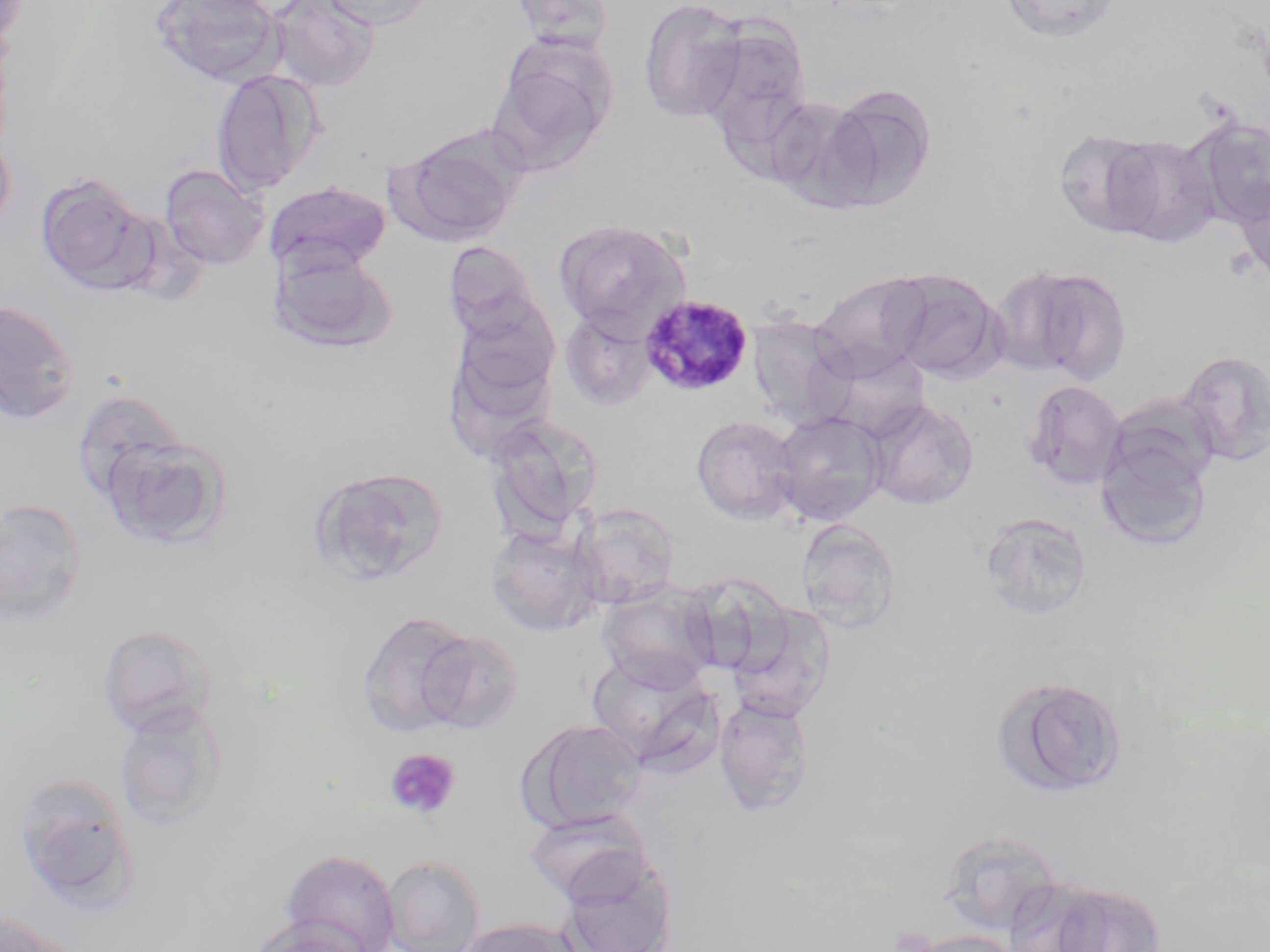

Approximate bounding boxes as (x1,y1)-(x2,y2) corner pairs in pixels. Plasmodium malariae-infected red blood cell locations: (639,294)-(754,397). Uninfected red blood cell locations: (265,0)-(380,93), (318,0)-(434,30), (509,0)-(617,53), (638,0)-(749,123), (1000,0)-(1122,43), (151,1)-(286,88), (691,17)-(813,142), (487,44)-(614,176), (211,69)-(325,195), (819,84)-(938,210), (1183,118)-(1270,228), (391,127)-(525,246), (1052,127)-(1166,238), (0,130)-(14,238), (1103,133)-(1223,247), (159,163)-(269,270), (36,173)-(159,296), (1231,175)-(1270,286), (264,180)-(391,274), (555,219)-(691,336), (443,242)-(543,342), (268,246)-(396,355), (995,264)-(1133,384), (878,268)-(1007,383), (810,272)-(934,381), (0,299)-(80,425), (560,309)-(658,410), (442,312)-(560,455), (746,314)-(856,428), (819,347)-(933,441), (1177,350)-(1270,467), (1022,380)-(1126,490), (69,387)-(195,508), (865,399)-(980,510), (771,410)-(890,526), (483,412)-(603,540), (1094,414)-(1218,552), (690,415)-(802,524), (98,433)-(229,549), (308,465)-(450,589), (0,499)-(88,628), (571,502)-(680,609), (979,511)-(1092,621), (795,518)-(902,632), (486,522)-(605,637), (677,574)-(792,679), (598,582)-(718,690), (724,602)-(836,722), (355,610)-(476,738), (97,624)-(219,737), (416,629)-(525,734), (586,650)-(721,770), (993,675)-(1130,797), (714,695)-(816,816), (114,701)-(229,831), (519,718)-(647,833), (14,772)-(136,906), (522,809)-(653,905), (937,829)-(1063,935), (281,850)-(401,952), (558,854)-(678,952), (381,855)-(486,952), (1000,878)-(1119,951), (1042,881)-(1167,951), (0,912)-(78,952), (458,917)-(585,952), (245,918)-(375,952), (907,930)-(1021,952). Platelet locations: (385,747)-(461,820), (886,928)-(938,952). Slide-level diagnosis: Plasmodium malariae. Image is 1270×952 pixels. Thin blood film. Optical microscopy. May-Grünwald-Giemsa stain. 1000x magnification. One field of a larger specimen.